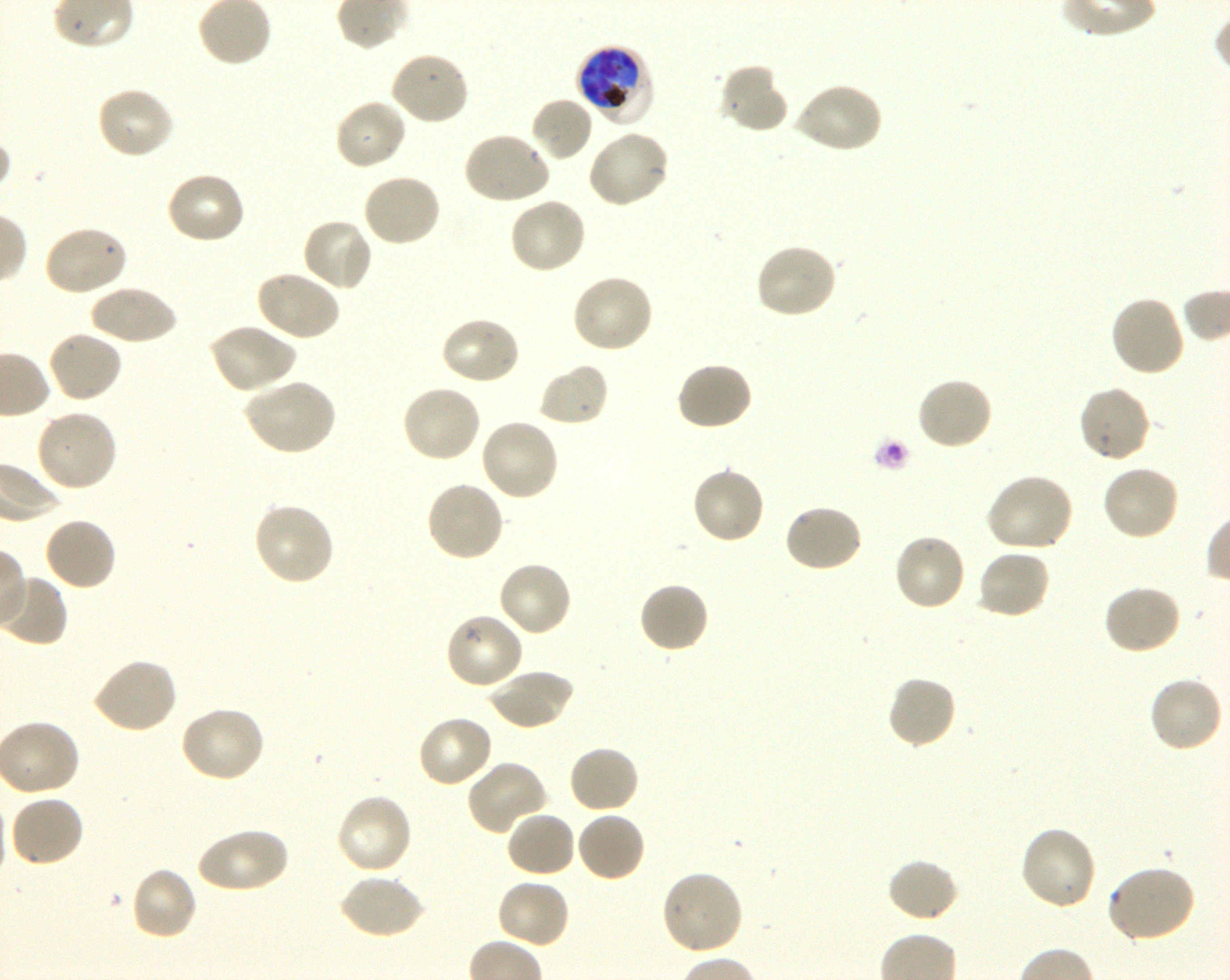
Approximate bounding boxes as (x1, y1, x2, y2) in pixels. Not every red blood cell is marked. A life-cycle stage — or a range of stages, where the recorded stages span more than one — follows each staged infected red blood cell. Locations of infected red blood cells: (575, 44, 653, 123) late trophozoite to late schizont. Locations of uninfected red blood cells: (389, 49, 471, 126), (718, 64, 789, 135), (792, 81, 883, 155), (94, 85, 176, 160), (530, 96, 594, 163), (333, 97, 408, 171), (586, 130, 671, 209), (462, 131, 552, 207), (165, 171, 246, 246), (361, 173, 442, 248), (507, 196, 587, 275), (301, 217, 375, 292), (42, 224, 128, 296), (754, 242, 839, 320), (254, 268, 341, 342), (569, 273, 654, 355), (89, 283, 177, 346), (1109, 296, 1186, 379), (439, 315, 522, 386), (208, 322, 297, 394), (46, 329, 123, 404), (675, 361, 754, 432), (537, 362, 610, 427), (244, 376, 337, 456), (915, 376, 994, 452), (1076, 384, 1151, 465), (400, 385, 482, 464), (33, 408, 119, 493), (479, 417, 560, 503), (690, 465, 767, 545), (1101, 465, 1181, 542), (985, 473, 1075, 553), (425, 479, 505, 563), (252, 501, 336, 587), (782, 503, 864, 573), (42, 515, 118, 591), (893, 532, 967, 613), (976, 548, 1052, 620), (497, 560, 573, 638), (637, 581, 710, 654), (1102, 584, 1182, 656), (444, 611, 525, 691), (90, 657, 178, 735), (488, 667, 574, 731), (885, 674, 958, 749), (1147, 674, 1225, 753), (178, 705, 266, 783), (416, 713, 494, 788), (567, 744, 640, 815), (465, 760, 548, 836), (335, 792, 414, 876), (7, 794, 85, 869), (505, 810, 577, 879), (576, 811, 647, 883), (1018, 824, 1098, 911), (196, 826, 289, 894), (886, 858, 961, 923), (1105, 865, 1197, 944), (130, 866, 198, 942), (659, 869, 744, 957), (339, 874, 425, 940), (495, 878, 571, 949). Giemsa-stained preparation. Thin blood smear. 100x objective under oil immersion, numerical aperture 1.30. Image is 1230×980 pixels. Shaking in-vitro culture of P. falciparum strain 3D7. Blood group of the donor: O+. Single field of view.